Classify this cell by malaria status.
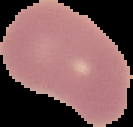
Uninfected.

Summary:
  - Image type: segmented cell region on a black background
  - Image size: 133×127 pixels
  - Preparation: thin blood smear